Assess this cell for malaria.
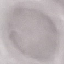

Uninfected.

Automatically extracted cell patch, resized to 64 × 64 pixels. Thin smear of blood. Giemsa stain. Photographed with a smartphone camera at the microscope eyepiece.